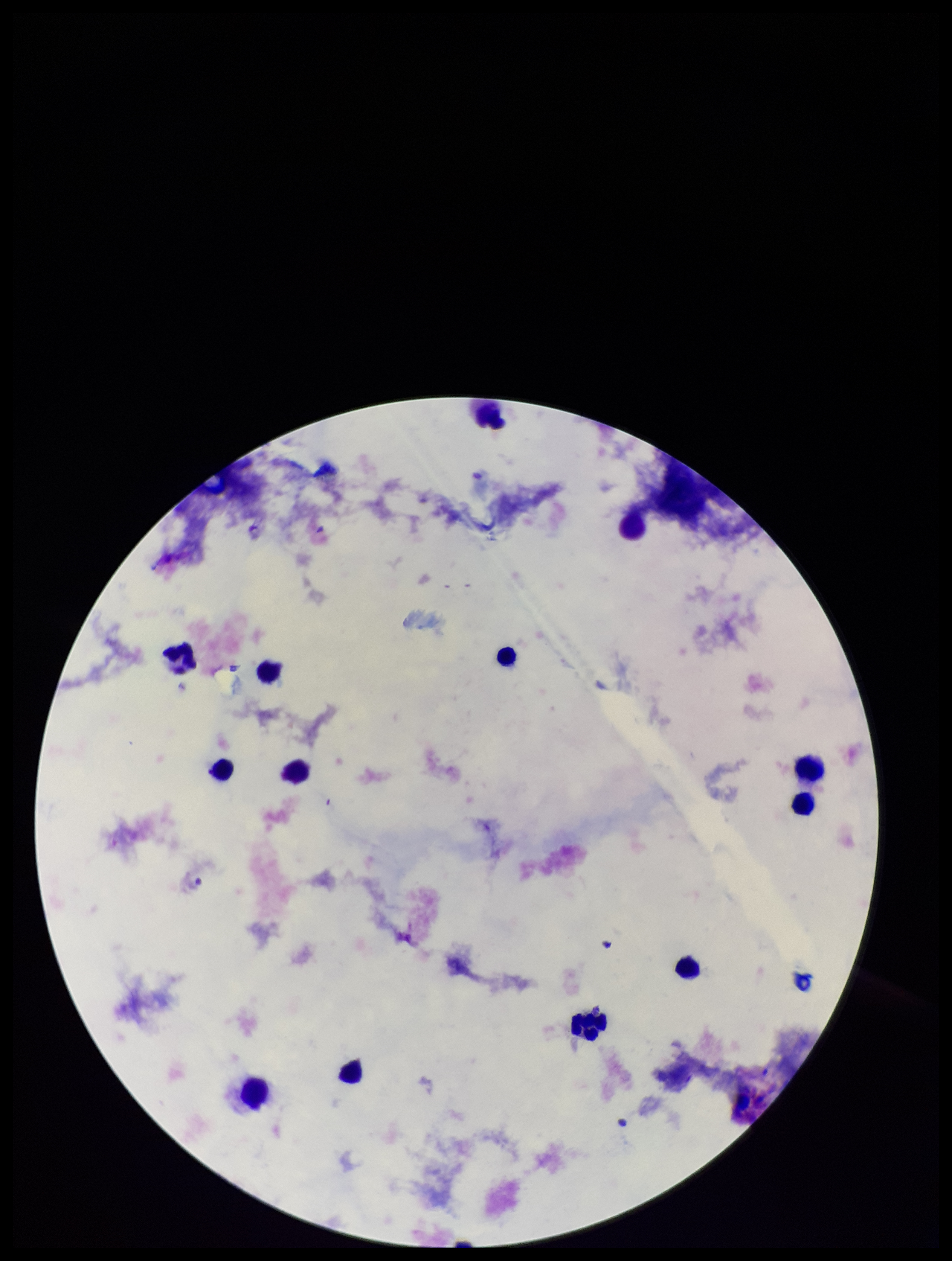

Summary:
  - Field of view: single
  - Patient malaria status: negative
  - Image size: 952×1261 pixels
  - Parasite count: 0
  - Stain: Giemsa
  - Capture: smartphone photograph through the microscope eyepiece
  - Preparation: thick blood smear
  - Leukocyte count: 13
  - Plasmodium parasites: none seen